Locate and identify every blood parasite.
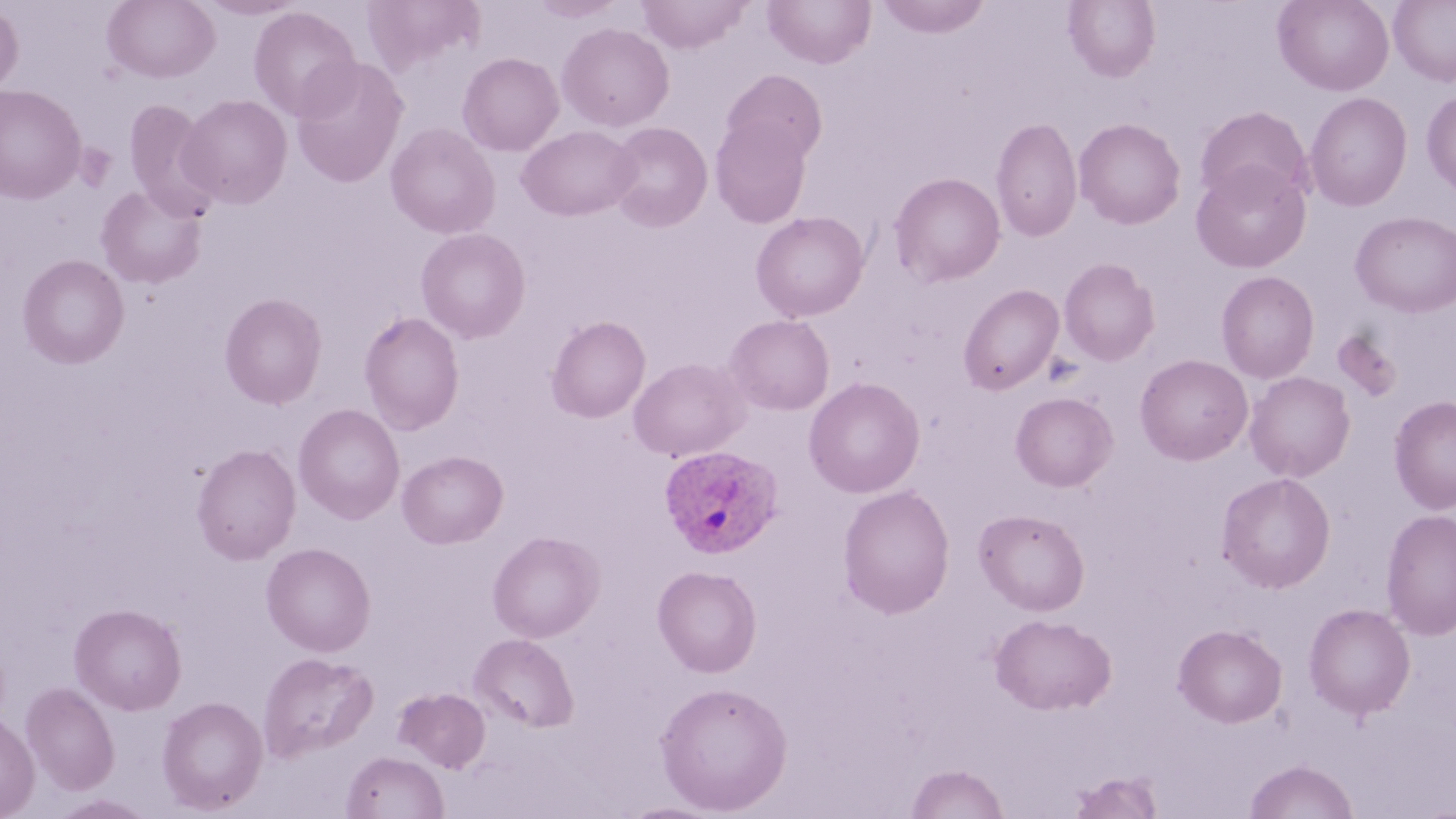
Approximate bounding boxes as named x1/y1/x2/y2 corners in pixels.
Plasmodium ovale-infected red blood cells: (x1=658, y1=444, x2=784, y2=558).
No Plasmodium falciparum, Plasmodium malariae, Plasmodium vivax, Babesia divergens, or Trypanosoma brucei observed.

Uninfected red blood cell locations: (x1=102, y1=0, x2=220, y2=83), (x1=197, y1=0, x2=306, y2=20), (x1=528, y1=0, x2=627, y2=22), (x1=636, y1=0, x2=752, y2=53), (x1=762, y1=0, x2=876, y2=68), (x1=874, y1=0, x2=993, y2=38), (x1=1273, y1=0, x2=1394, y2=95), (x1=1389, y1=0, x2=1456, y2=86), (x1=1064, y1=1, x2=1160, y2=81), (x1=0, y1=3, x2=24, y2=96), (x1=248, y1=6, x2=361, y2=121), (x1=557, y1=22, x2=674, y2=131), (x1=457, y1=52, x2=564, y2=156), (x1=290, y1=56, x2=409, y2=188), (x1=721, y1=69, x2=828, y2=164), (x1=0, y1=84, x2=86, y2=204), (x1=1421, y1=88, x2=1456, y2=198), (x1=1305, y1=92, x2=1413, y2=211), (x1=177, y1=94, x2=292, y2=209), (x1=123, y1=99, x2=218, y2=217), (x1=1194, y1=105, x2=1313, y2=207), (x1=711, y1=116, x2=812, y2=227), (x1=991, y1=116, x2=1082, y2=243), (x1=1074, y1=117, x2=1186, y2=229), (x1=606, y1=122, x2=713, y2=232), (x1=386, y1=123, x2=500, y2=238), (x1=403, y1=123, x2=511, y2=339), (x1=517, y1=125, x2=640, y2=221), (x1=1191, y1=160, x2=1311, y2=272), (x1=889, y1=173, x2=1005, y2=287), (x1=96, y1=185, x2=206, y2=289), (x1=751, y1=211, x2=870, y2=322), (x1=1351, y1=211, x2=1456, y2=316), (x1=415, y1=227, x2=530, y2=343), (x1=17, y1=254, x2=129, y2=369), (x1=1059, y1=257, x2=1160, y2=366), (x1=1216, y1=271, x2=1319, y2=383), (x1=958, y1=284, x2=1064, y2=395), (x1=219, y1=293, x2=327, y2=409), (x1=358, y1=311, x2=465, y2=435), (x1=724, y1=314, x2=835, y2=415), (x1=546, y1=316, x2=651, y2=422), (x1=1331, y1=330, x2=1403, y2=403), (x1=1135, y1=354, x2=1253, y2=465), (x1=628, y1=357, x2=749, y2=462), (x1=1244, y1=371, x2=1355, y2=482), (x1=804, y1=376, x2=925, y2=498), (x1=1011, y1=391, x2=1118, y2=491), (x1=1388, y1=395, x2=1456, y2=514), (x1=294, y1=403, x2=404, y2=523), (x1=191, y1=443, x2=302, y2=564), (x1=397, y1=450, x2=508, y2=549), (x1=1216, y1=472, x2=1336, y2=593), (x1=838, y1=484, x2=956, y2=619), (x1=1380, y1=508, x2=1456, y2=639), (x1=974, y1=509, x2=1089, y2=615), (x1=487, y1=530, x2=604, y2=643), (x1=261, y1=542, x2=376, y2=656), (x1=652, y1=565, x2=762, y2=677), (x1=69, y1=603, x2=187, y2=715), (x1=1303, y1=603, x2=1416, y2=720), (x1=990, y1=613, x2=1116, y2=714), (x1=1173, y1=624, x2=1287, y2=727), (x1=469, y1=633, x2=579, y2=732), (x1=258, y1=652, x2=378, y2=762), (x1=655, y1=681, x2=792, y2=814), (x1=21, y1=682, x2=119, y2=794), (x1=394, y1=687, x2=490, y2=773), (x1=157, y1=696, x2=268, y2=813), (x1=0, y1=711, x2=39, y2=819), (x1=342, y1=751, x2=448, y2=819), (x1=1244, y1=759, x2=1359, y2=818), (x1=905, y1=763, x2=1009, y2=819), (x1=1068, y1=771, x2=1164, y2=819), (x1=50, y1=794, x2=157, y2=818), (x1=617, y1=801, x2=725, y2=818). Slide-level diagnosis: Plasmodium ovale. Thin blood film. Single field of view. Image is 1456×819 pixels. May-Grünwald-Giemsa stain. Light microscopy. 1000x magnification.